Assess the background quality.
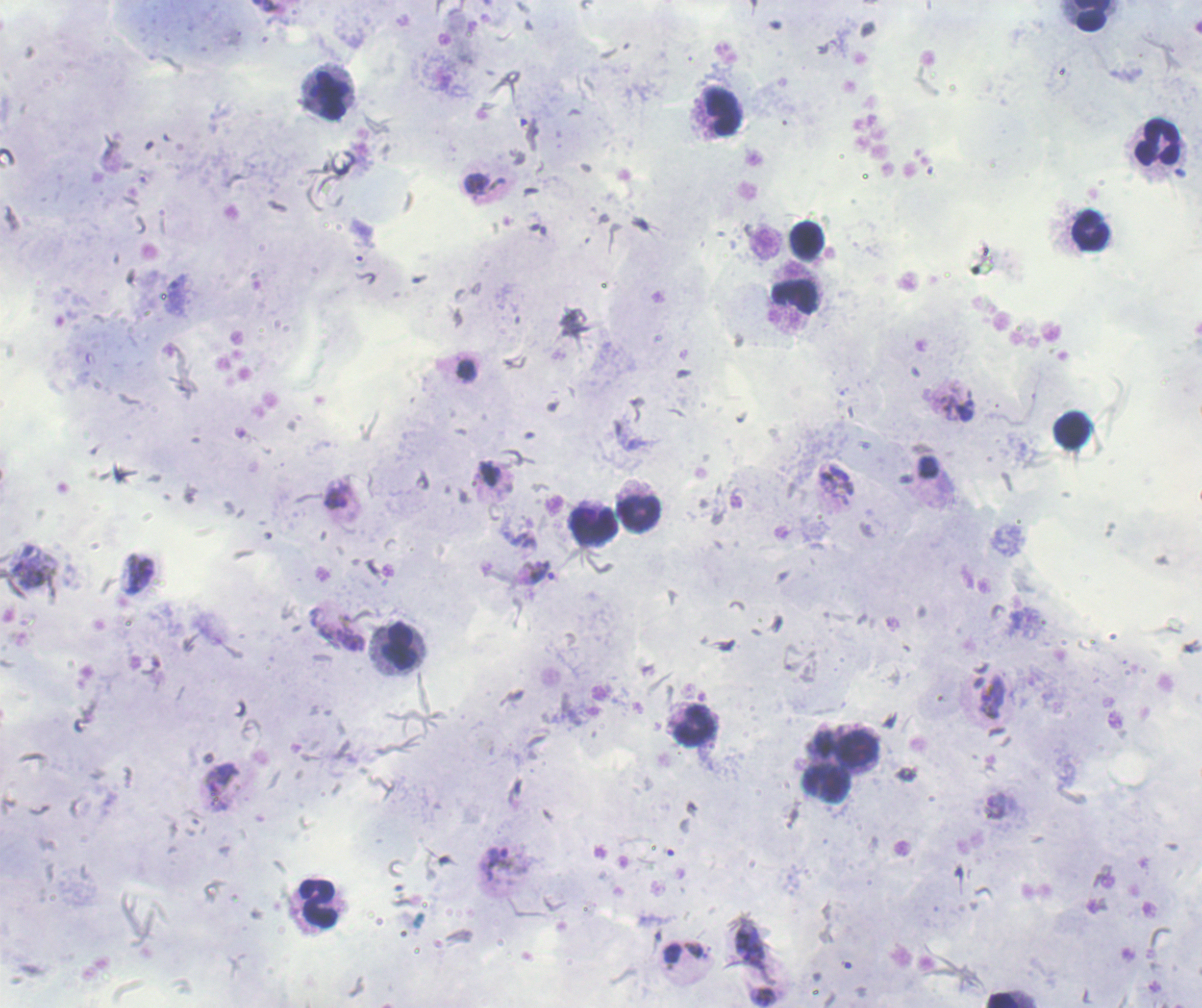

Good.

{
  "preparation": "thick blood smear",
  "field_of_view": "one from this slide",
  "context": "previously used in an actual diagnosis",
  "result": "positive for Plasmodium parasites",
  "leukocyte_locations": "approximate object centers, in pixels from the top-left corner: (x=1092, y=15), (x=328, y=94), (x=722, y=110), (x=1158, y=144), (x=1092, y=231), (x=805, y=240), (x=795, y=296), (x=1073, y=430), (x=638, y=512), (x=594, y=524), (x=399, y=646), (x=694, y=727), (x=857, y=749), (x=827, y=784), (x=318, y=905), (x=1003, y=1000)",
  "image_size": "1202×1008 pixels",
  "magnification": "100x",
  "stain": "Romanowsky",
  "trophozoite_locations": "approximate object centers, in pixels from the top-left corner: (x=476, y=185), (x=467, y=371), (x=489, y=473), (x=336, y=500), (x=541, y=573), (x=138, y=574), (x=992, y=698), (x=222, y=786), (x=497, y=863), (x=750, y=942)"
}